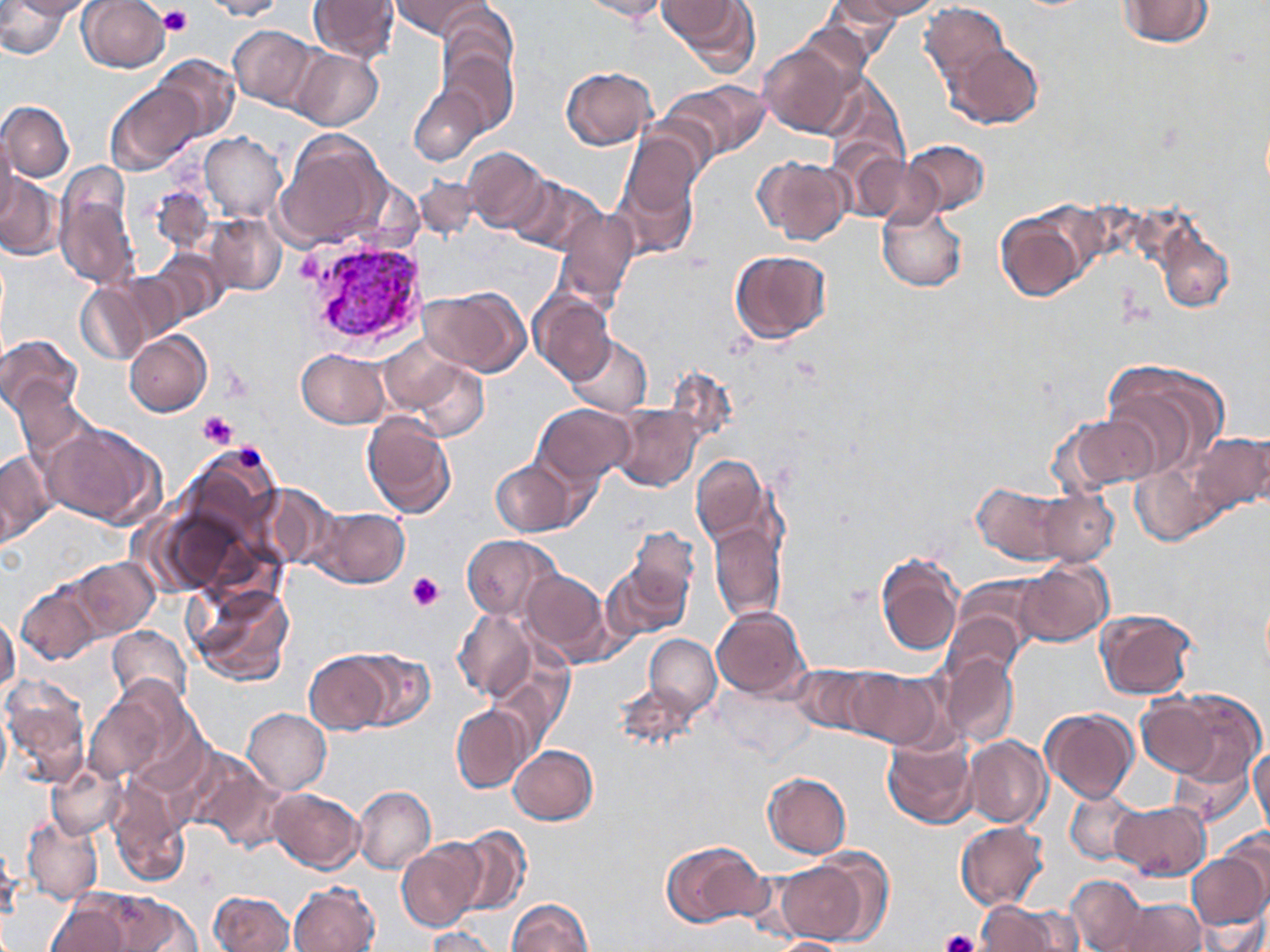
{
  "slide_level_diagnosis": "Plasmodium vivax",
  "field_of_view": "single",
  "preparation": "thin blood smear",
  "uninfected_red_blood_cell_locations": "approximate bounding boxes as [x1, y1, x2, y2] in pixels: [9, 0, 89, 19], [78, 0, 170, 72], [199, 0, 289, 20], [310, 0, 399, 64], [391, 0, 488, 38], [579, 0, 673, 22], [834, 0, 938, 23], [1113, 0, 1217, 49], [0, 1, 73, 59], [658, 1, 759, 68], [824, 1, 921, 43], [919, 1, 1014, 92], [438, 5, 518, 85], [228, 24, 320, 110], [757, 35, 866, 139], [949, 42, 1044, 129], [293, 48, 383, 130], [442, 51, 518, 135], [155, 54, 241, 142], [560, 65, 658, 150], [822, 74, 908, 182], [665, 79, 770, 163], [109, 80, 198, 174], [410, 85, 486, 166], [0, 101, 74, 181], [276, 129, 386, 251], [0, 131, 17, 227], [199, 133, 286, 222], [901, 139, 989, 216], [613, 142, 702, 258], [836, 144, 925, 221], [461, 147, 550, 235], [753, 154, 852, 245], [865, 158, 942, 229], [0, 172, 64, 261], [54, 172, 143, 292], [417, 177, 482, 242], [511, 177, 608, 256], [149, 185, 215, 256], [877, 202, 969, 293], [995, 207, 1091, 305], [556, 208, 637, 310], [203, 215, 286, 297], [1156, 217, 1238, 314], [150, 248, 227, 325], [729, 248, 832, 345], [111, 272, 190, 347], [75, 281, 151, 364], [421, 286, 530, 376], [530, 288, 616, 385], [124, 332, 211, 417], [0, 334, 84, 422], [565, 335, 652, 417], [298, 349, 390, 428], [401, 354, 490, 443], [1101, 360, 1228, 476], [13, 379, 94, 471], [611, 403, 703, 493], [534, 404, 636, 487], [1051, 411, 1163, 498], [362, 412, 457, 518], [43, 422, 165, 529], [1187, 430, 1270, 519], [0, 450, 55, 545], [690, 455, 771, 549], [491, 460, 576, 534], [1131, 463, 1214, 546], [972, 481, 1074, 565], [259, 484, 342, 572], [1037, 489, 1118, 567], [308, 506, 410, 588], [710, 523, 784, 622], [625, 525, 701, 617], [460, 534, 563, 621], [875, 552, 965, 656], [68, 557, 159, 641], [603, 559, 690, 641], [1017, 560, 1112, 647], [522, 567, 616, 666], [949, 576, 1047, 665], [17, 582, 102, 664], [189, 582, 294, 685], [711, 604, 811, 701], [1095, 608, 1198, 700], [454, 609, 535, 701], [0, 610, 18, 699], [943, 610, 1025, 690], [108, 625, 191, 710], [645, 634, 720, 719], [350, 650, 435, 730], [304, 652, 392, 734], [942, 653, 1018, 747], [488, 663, 569, 755], [792, 665, 878, 738], [844, 666, 944, 750], [2, 676, 88, 786], [615, 677, 706, 751], [82, 685, 179, 787], [1137, 689, 1258, 790], [451, 705, 528, 793], [1041, 707, 1138, 801], [243, 708, 331, 794], [0, 711, 11, 788], [882, 731, 978, 830], [964, 735, 1052, 828], [508, 743, 599, 825], [1250, 746, 1269, 832], [192, 753, 291, 851], [49, 761, 126, 841], [761, 772, 851, 859], [351, 784, 435, 873], [269, 788, 364, 874], [1066, 788, 1144, 864], [108, 790, 186, 888], [1110, 800, 1210, 880], [22, 814, 103, 906], [955, 822, 1049, 908], [451, 825, 530, 916], [1218, 830, 1270, 911], [396, 838, 486, 932], [661, 838, 771, 927], [0, 842, 22, 922], [1188, 850, 1270, 929], [774, 851, 880, 946], [1068, 875, 1150, 950], [290, 879, 380, 952], [68, 891, 202, 952], [207, 891, 296, 951], [45, 897, 136, 952], [1102, 897, 1208, 952], [507, 898, 593, 951], [976, 901, 1067, 951], [1198, 911, 1268, 952], [424, 927, 501, 952], [766, 936, 851, 951]",
  "modality": "light microscopy",
  "plasmodium_vivax_infected_red_blood_cell_locations": "approximate bounding boxes as [x1, y1, x2, y2] in pixels: [298, 236, 426, 353]",
  "platelet_locations": "approximate bounding boxes as [x1, y1, x2, y2] in pixels: [158, 4, 195, 37], [295, 249, 323, 280], [198, 410, 238, 449], [234, 446, 265, 473], [407, 572, 444, 611], [941, 928, 979, 952]",
  "stain": "May-Grünwald-Giemsa",
  "image_size": "1270×952 pixels",
  "magnification": "1000x"
}